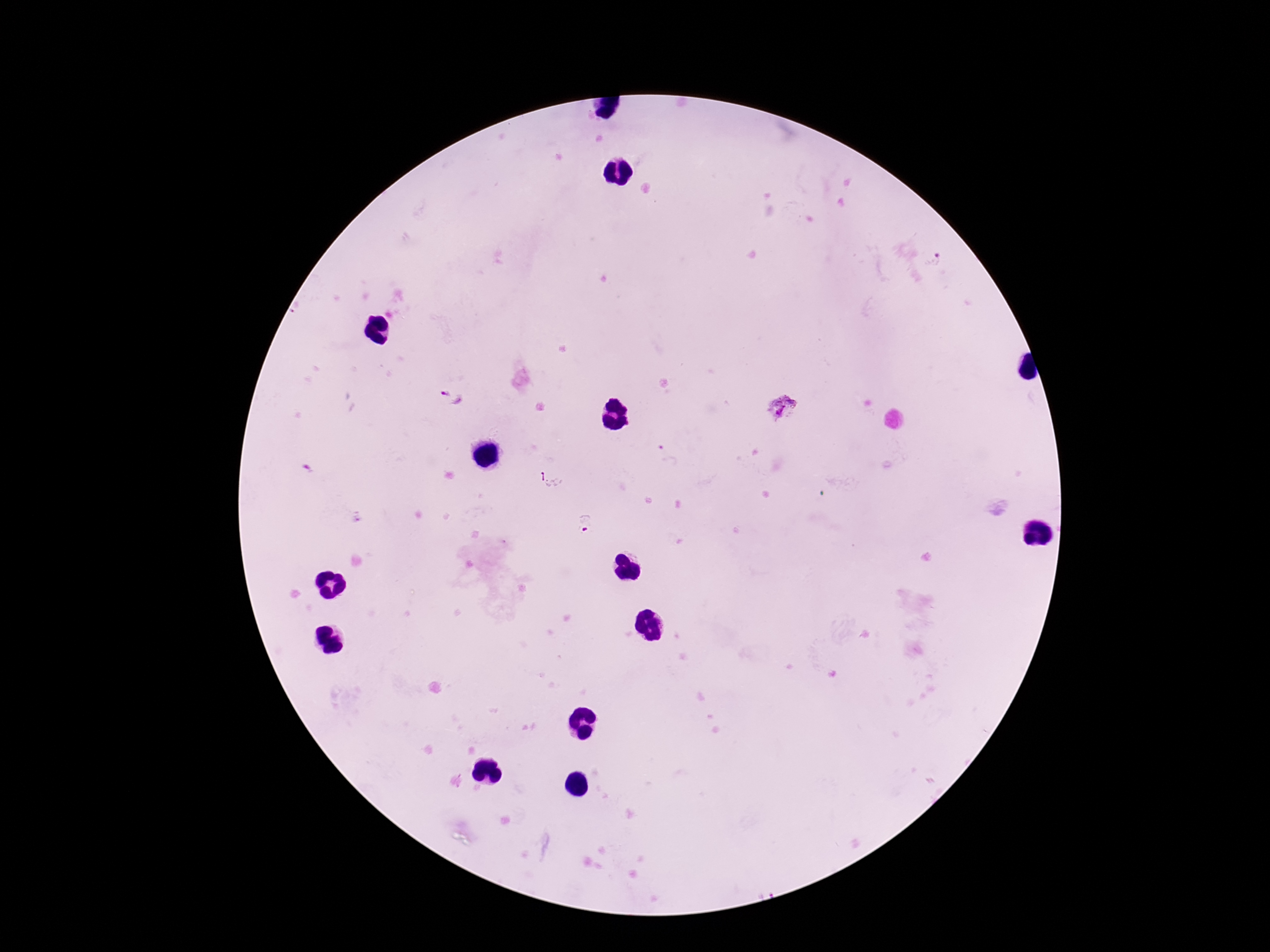
Plasmodium parasite locations = approximate centers as {x, y} in pixels: {936, 260}, {453, 398}, {782, 409}, {307, 471}, {552, 479}, {585, 523}
field of view = single
patient malaria status = positive
stain = Giemsa
preparation = thick blood smear
magnification = 100x
image size = 1270×952 pixels
capture = smartphone camera through the microscope eyepiece